Comment on the morphology of the red blood cells.
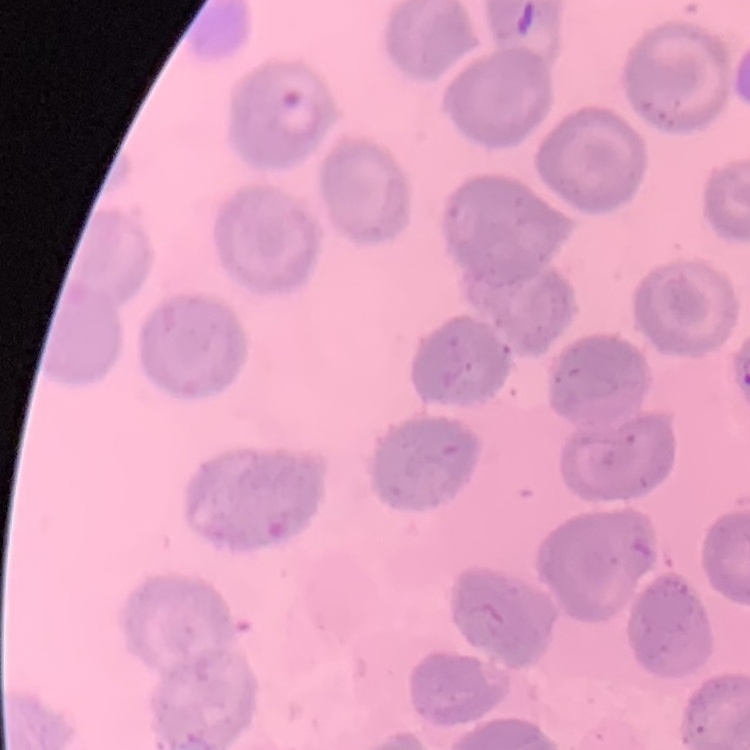

They show no rouleaux formation.

Summary:
  - Stain: Field's or Giemsa
  - Image type: one tile cut from a larger photomicrograph
  - Preparation: thin peripheral smear